Identify the parasite.
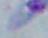

This is Toxoplasma gondii.

modality: micrograph
magnification: 1000x